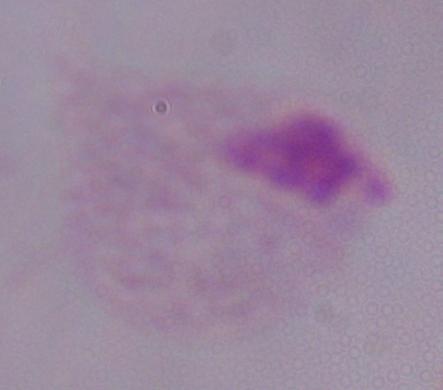
{
  "modality": "photomicrograph",
  "magnification": "1000x",
  "identification": "trichomonad"
}